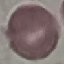
Summary:
  - Malaria status: uninfected
  - Stain: Giemsa
  - Capture: smartphone camera at the microscope eyepiece
  - Image type: automatically extracted cell patch, resized to 64 × 64 pixels
  - Preparation: thin blood film